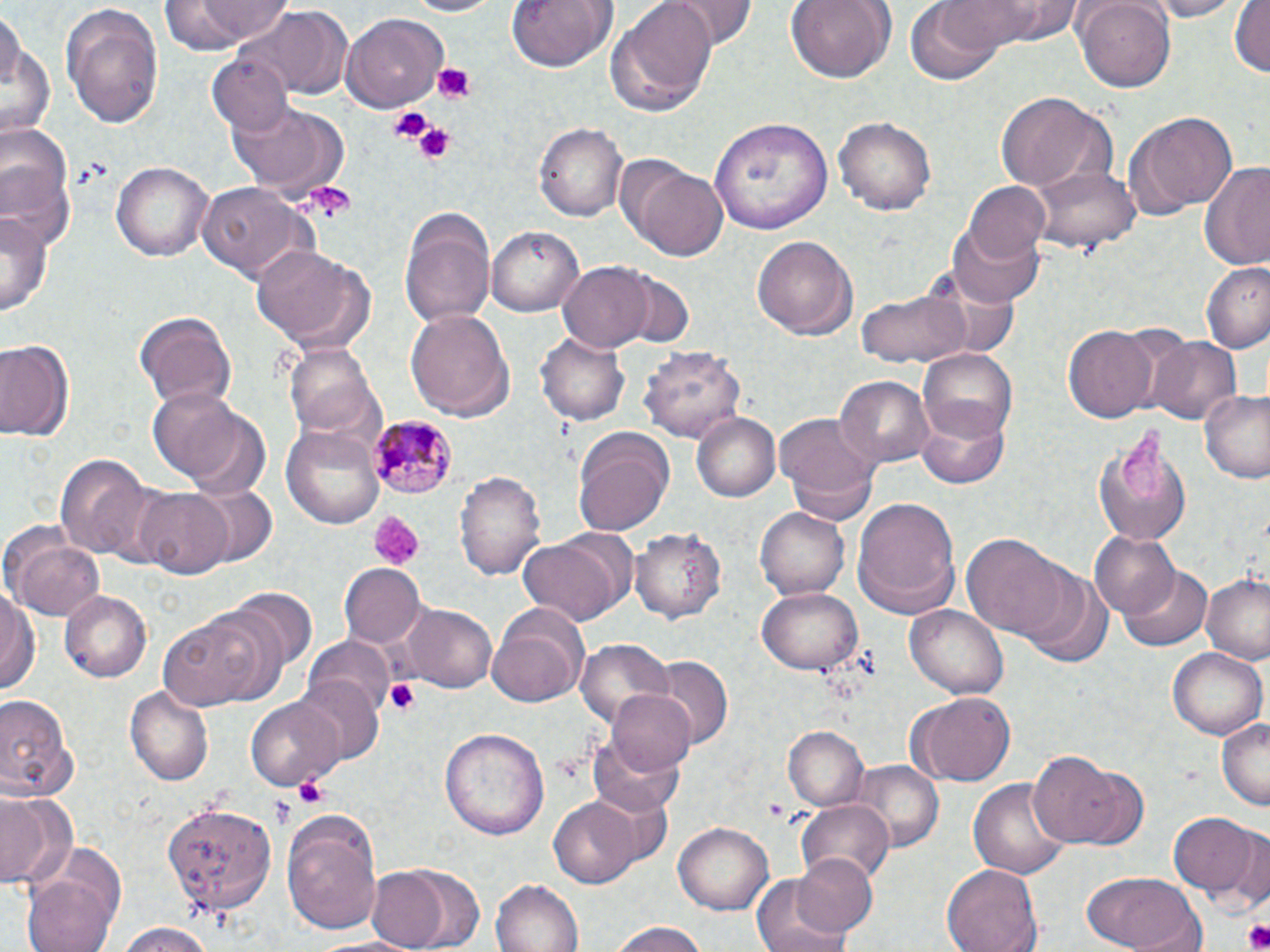

Summary:
  - Coordinate format: approximate bounding boxes as (x1,y1)-(x2,y2) corner pairs in pixels
  - Plasmodium malariae-infected red blood cell locations: (369,416)-(458,499)
  - Uninfected red blood cell locations: (160,0)-(293,51), (400,0)-(504,17), (506,0)-(613,75), (608,0)-(716,113), (668,0)-(754,49), (786,0)-(892,83), (939,0)-(1073,46), (1070,0)-(1176,91), (1141,0)-(1244,22), (1229,0)-(1269,80), (905,1)-(1011,86), (60,4)-(165,130), (243,7)-(354,98), (340,13)-(448,112), (1,20)-(55,142), (206,53)-(294,136), (997,90)-(1116,194), (228,100)-(350,200), (1130,111)-(1237,216), (834,114)-(938,216), (709,115)-(834,232), (534,121)-(627,223), (1165,128)-(1265,257), (1,134)-(75,252), (111,161)-(212,263), (1199,161)-(1270,270), (631,162)-(728,261), (1032,162)-(1138,251), (962,179)-(1051,265), (195,180)-(314,285), (397,206)-(497,329), (0,207)-(49,317), (946,221)-(1045,309), (489,227)-(584,317), (752,236)-(858,344), (251,243)-(373,352), (559,260)-(655,351), (1201,263)-(1270,353), (923,264)-(1023,361), (622,269)-(691,347), (857,290)-(969,366), (406,309)-(515,421), (133,310)-(236,408), (1064,324)-(1161,422), (536,327)-(630,426), (1148,334)-(1242,425), (1,337)-(75,445), (285,345)-(384,442), (641,345)-(745,448), (918,347)-(1019,440), (834,375)-(935,471), (148,390)-(271,494), (1199,390)-(1270,484), (916,406)-(1010,489), (690,412)-(782,502), (775,412)-(882,523), (1091,423)-(1196,549), (283,425)-(385,529), (574,427)-(676,536), (55,453)-(154,561), (455,471)-(546,582), (131,485)-(234,578), (184,485)-(277,568), (852,496)-(961,619), (755,506)-(850,600), (5,525)-(104,623), (631,525)-(726,623), (1089,531)-(1181,621), (961,532)-(1071,642), (518,535)-(627,627), (1019,561)-(1114,667), (340,564)-(427,651), (1121,564)-(1213,652), (1202,568)-(1270,664), (0,582)-(40,702), (227,586)-(318,676), (758,586)-(863,672), (59,590)-(152,684), (486,603)-(591,709), (905,603)-(1008,698), (403,605)-(498,694), (157,609)-(288,712), (302,637)-(394,719), (576,638)-(676,735), (1167,648)-(1265,738), (653,656)-(732,753), (295,676)-(383,767), (124,685)-(213,786), (607,687)-(694,779), (910,692)-(1014,785), (0,693)-(81,804), (246,697)-(341,788), (1217,718)-(1269,809), (783,726)-(868,813), (440,727)-(549,840), (589,731)-(684,820), (1029,749)-(1135,846), (849,761)-(942,851), (971,773)-(1071,879), (0,792)-(74,890), (549,798)-(644,887), (163,800)-(277,917), (795,800)-(894,886), (280,809)-(384,933), (1169,811)-(1259,897), (672,822)-(774,916), (1224,824)-(1268,910), (789,850)-(879,940), (364,863)-(461,952), (942,863)-(1043,952), (23,870)-(120,952), (1081,871)-(1207,952), (750,874)-(854,952), (491,876)-(585,951), (110,922)-(222,951), (607,925)-(713,952)
  - Platelet locations: (431,64)-(478,104), (388,107)-(432,145), (413,122)-(459,166), (304,182)-(356,221), (369,511)-(422,568), (385,679)-(421,717), (293,776)-(332,809), (268,792)-(296,828), (1241,921)-(1270,952)
  - Slide-level diagnosis: Plasmodium malariae
  - Image size: 1270×952 pixels
  - Stain: May-Grünwald-Giemsa
  - Field of view: one of a larger specimen
  - Preparation: thin blood film
  - Modality: light microscopy
  - Magnification: 1000x